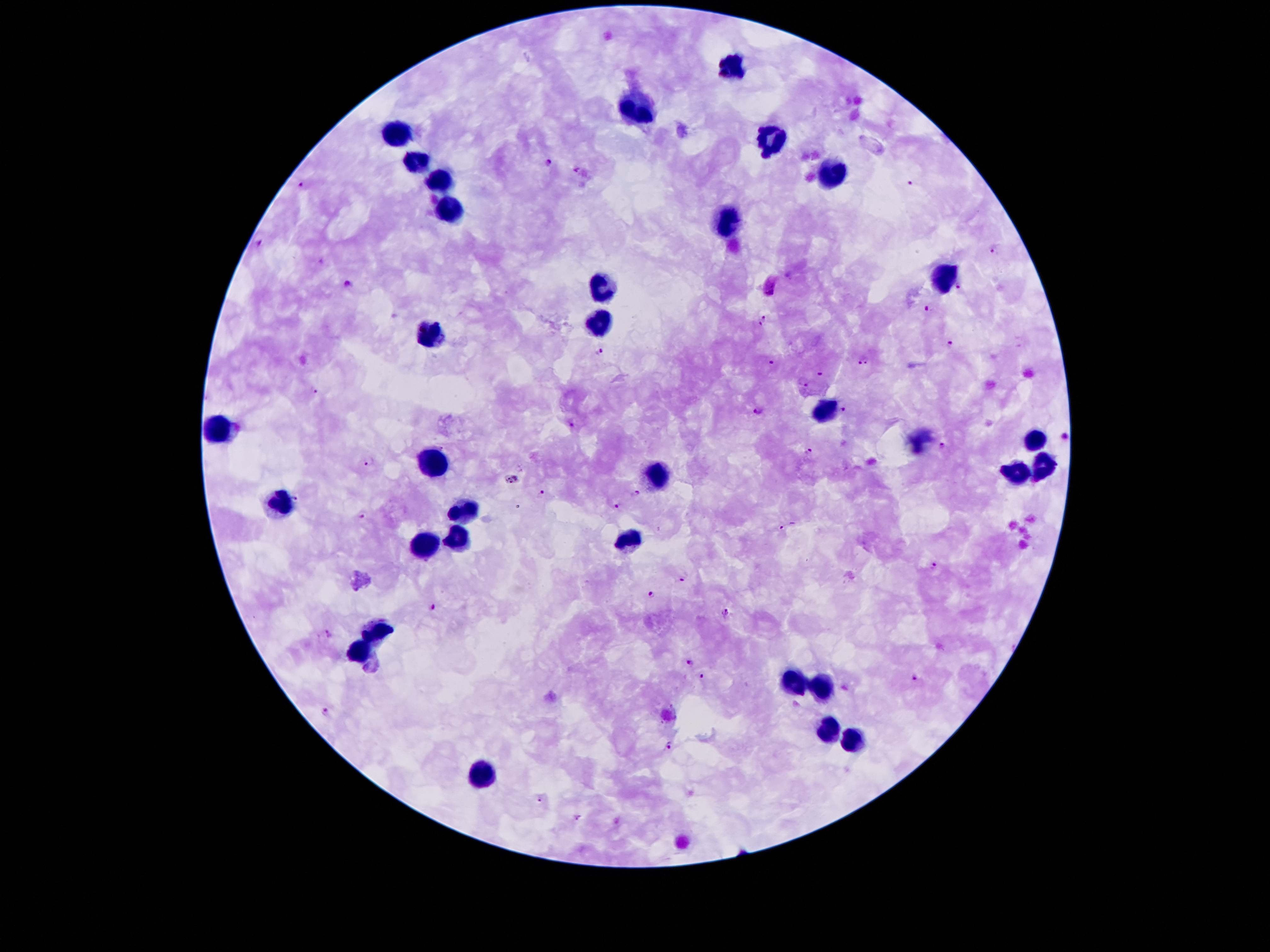

Approximate object centers, in pixels from the top-left corner.
Summary:
  - Leukocyte locations: (x=732, y=65), (x=640, y=105), (x=399, y=132), (x=770, y=138), (x=418, y=162), (x=836, y=170), (x=443, y=180), (x=453, y=211), (x=729, y=221), (x=942, y=278), (x=603, y=286), (x=600, y=322), (x=432, y=336), (x=825, y=409), (x=218, y=428), (x=1036, y=439), (x=435, y=461), (x=1041, y=466), (x=656, y=473), (x=1017, y=474), (x=280, y=503), (x=464, y=507), (x=456, y=536), (x=630, y=539), (x=424, y=544), (x=380, y=629), (x=359, y=652), (x=793, y=682), (x=824, y=690), (x=827, y=731), (x=855, y=742), (x=483, y=774)
  - Plasmodium parasite locations: (x=548, y=162), (x=910, y=181), (x=299, y=184), (x=260, y=242), (x=992, y=249), (x=348, y=285), (x=960, y=286), (x=928, y=310), (x=764, y=320), (x=947, y=344), (x=597, y=351), (x=864, y=360), (x=770, y=362), (x=821, y=370), (x=802, y=383), (x=315, y=392), (x=757, y=409), (x=844, y=409), (x=941, y=445), (x=809, y=449), (x=369, y=462), (x=513, y=478), (x=541, y=493), (x=634, y=495), (x=298, y=498), (x=619, y=506), (x=361, y=516), (x=783, y=529), (x=935, y=567), (x=683, y=579), (x=651, y=595), (x=434, y=605), (x=727, y=611), (x=329, y=632), (x=690, y=662), (x=701, y=675), (x=917, y=677), (x=326, y=713), (x=669, y=745), (x=540, y=799)
  - Image size: 1270×952 pixels
  - Capture: smartphone camera through the microscope eyepiece
  - Field of view: single
  - Stain: Giemsa
  - Magnification: 100x
  - Patient malaria status: infected with Plasmodium falciparum
  - Preparation: thick blood smear